Name the cell type shown.
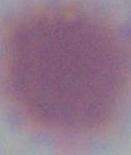

An erythrocyte.

Summary:
  - Magnification: 1000x
  - Modality: photomicrograph